Identify the cell.
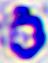

A leukocyte.

modality = photomicrograph
magnification = 400x